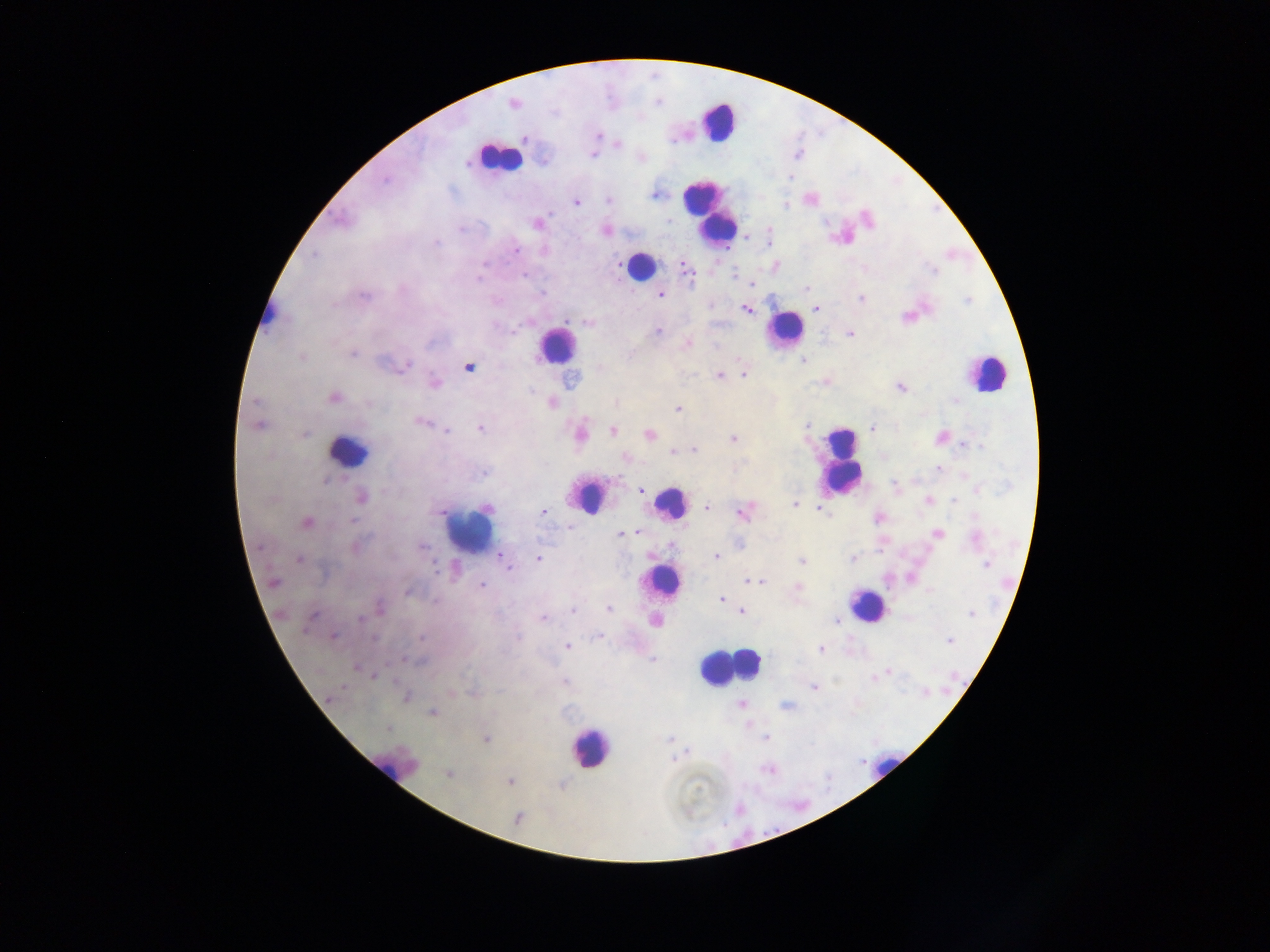
Approximate centers as {x, y} in pixels.
Summary:
  - Leukocyte locations: {717, 122}, {498, 157}, {709, 211}, {639, 266}, {268, 314}, {784, 330}, {556, 346}, {985, 373}, {349, 451}, {842, 460}, {588, 497}, {670, 502}, {470, 531}, {665, 582}, {866, 605}, {749, 663}, {726, 668}, {590, 748}, {392, 765}, {881, 767}
  - Malaria parasite locations: {513, 103}, {598, 136}, {525, 139}, {672, 141}, {618, 144}, {592, 155}, {543, 161}, {466, 164}, {790, 177}, {385, 179}, {654, 195}, {609, 200}, {576, 203}, {785, 205}, {550, 214}, {867, 218}, {670, 220}, {537, 224}, {768, 227}, {460, 229}, {606, 230}, {436, 243}, {515, 250}, {314, 255}, {483, 265}, {776, 267}, {687, 269}, {934, 271}, {735, 275}, {525, 276}, {478, 279}, {752, 284}, {807, 288}, {542, 293}, {661, 295}, {862, 299}, {363, 301}, {816, 308}, {746, 310}, {587, 323}, {513, 332}, {656, 332}, {851, 334}, {687, 343}, {354, 353}, {302, 357}, {804, 361}, {406, 365}, {469, 367}, {744, 374}, {718, 375}, {435, 383}, {901, 387}, {334, 398}, {954, 400}, {255, 401}, {552, 403}, {615, 403}, {678, 409}, {420, 422}, {258, 426}, {807, 426}, {871, 428}, {480, 429}, {447, 431}, {613, 431}, {304, 434}, {581, 434}, {649, 434}, {939, 437}, {733, 439}, {963, 444}, {980, 446}, {695, 450}, {673, 451}, {626, 459}, {938, 469}, {484, 473}, {325, 480}, {894, 484}, {640, 491}, {362, 497}, {928, 500}, {954, 501}, {794, 504}, {706, 507}, {487, 508}, {821, 509}, {544, 512}, {743, 513}, {878, 517}, {974, 517}, {352, 521}, {306, 523}, {635, 532}, {938, 533}, {622, 534}, {975, 538}, {672, 545}, {421, 546}, {355, 547}, {499, 556}, {716, 556}, {538, 558}, {853, 559}, {299, 560}, {801, 561}, {986, 564}, {507, 566}, {435, 570}, {750, 581}, {273, 582}, {760, 582}, {482, 586}, {798, 588}, {930, 590}, {407, 592}, {721, 599}, {380, 607}, {609, 609}, {573, 610}, {742, 612}, {971, 614}, {311, 618}, {543, 618}, {360, 619}, {835, 620}, {600, 636}, {334, 637}, {421, 637}, {374, 638}, {949, 641}, {567, 646}, {821, 650}, {652, 659}, {409, 660}, {356, 667}, {888, 672}, {374, 676}, {565, 681}, {814, 687}, {926, 692}, {405, 697}, {329, 698}, {741, 705}, {786, 706}, {432, 713}, {388, 728}, {766, 738}, {486, 739}, {668, 739}, {674, 759}, {768, 770}, {448, 774}, {510, 782}, {518, 817}
  - Image size: 1270×952 pixels
  - Capture: mobile-phone photograph through a microscope
  - Country: Ghana
  - Field of view: single
  - Preparation: thick blood film